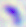 Micrograph. Toxoplasma gondii is seen. 400x magnification.